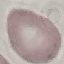
Summary:
  - Malaria status: uninfected
  - Image type: automatically extracted cell patch, resized to 64 × 64 pixels
  - Preparation: thin smear
  - Capture: smartphone camera at the microscope eyepiece
  - Stain: Giemsa